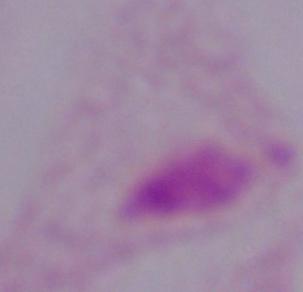

Summary:
  - Modality: photomicrograph
  - Identification: trichomonad
  - Magnification: 1000x